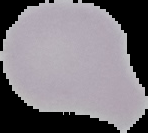
image size = 148×133 pixels
image type = segmented cell region on a black background
malaria status = uninfected
preparation = thin blood smear